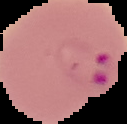

preparation = thin blood film
image size = 127×124 pixels
image type = segmented cell region with the area outside set to black
malaria status = parasitized